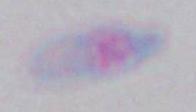

Photomicrograph. Toxoplasma gondii is shown. Captured at 1000x magnification.